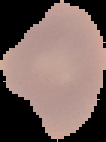 Cell region segmented out of the field of view; the surrounding area is masked to black. Image is 106×142 pixels. From a thin blood smear. Malaria status: uninfected.